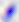
Summary:
  - Modality: micrograph
  - Identification: Toxoplasma gondii
  - Magnification: 400x